Assess the morphology of the red blood cells.
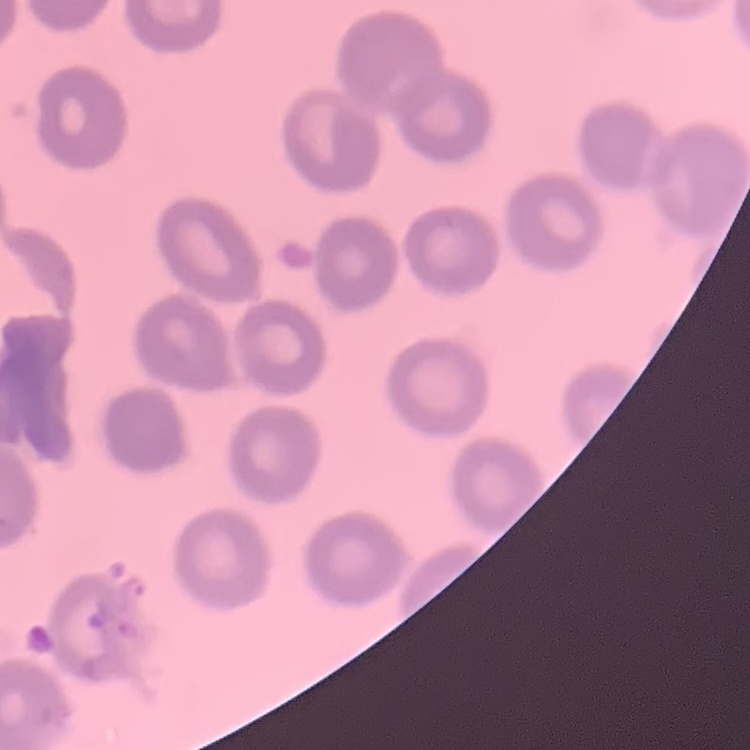
No rouleaux formation.

One tile cut from a larger photomicrograph. Stained with either Field's or Giemsa. Thin blood film.